State the blood parasite species.
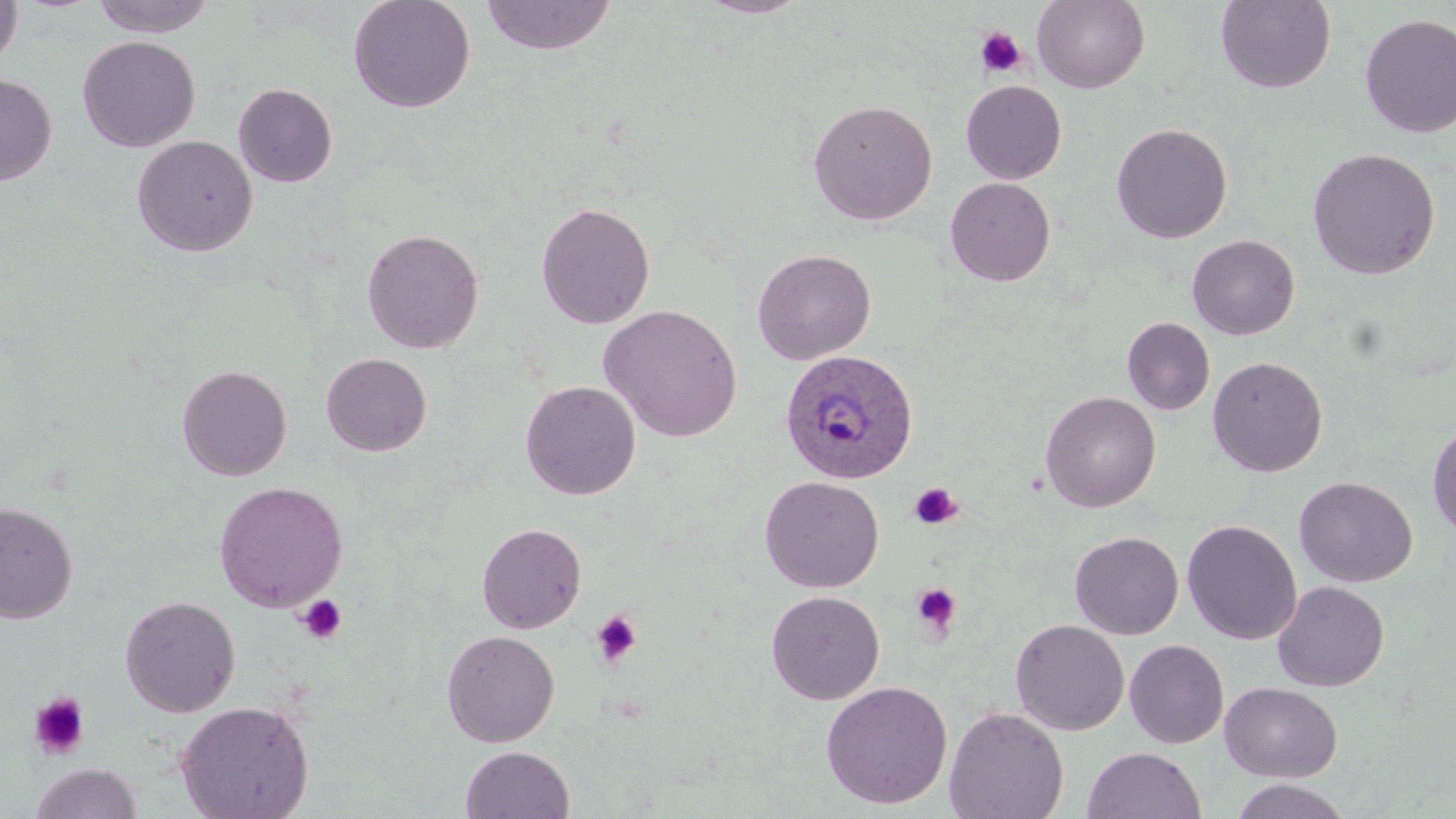
Plasmodium ovale.

Summary:
  - Coordinate format: approximate bounding boxes as [x1, y1, x2, y2] in pixels
  - Uninfected red blood cell locations: [0, 0, 23, 72], [90, 0, 218, 38], [348, 0, 476, 113], [481, 0, 617, 57], [694, 0, 813, 19], [1032, 0, 1150, 93], [1215, 1, 1336, 93], [1359, 13, 1456, 138], [77, 36, 201, 152], [0, 73, 57, 185], [961, 81, 1066, 184], [233, 83, 338, 187], [807, 98, 938, 226], [1111, 122, 1233, 244], [131, 135, 258, 256], [1306, 147, 1441, 280], [944, 177, 1055, 286], [535, 201, 656, 329], [361, 228, 485, 355], [1187, 234, 1300, 340], [752, 248, 877, 364], [599, 304, 742, 443], [1122, 317, 1215, 416], [320, 353, 432, 456], [1207, 355, 1328, 477], [176, 364, 293, 481], [520, 380, 641, 500], [1041, 390, 1161, 512], [1427, 419, 1456, 540], [759, 476, 884, 593], [1294, 476, 1418, 588], [213, 480, 349, 612], [0, 500, 78, 623], [1182, 519, 1302, 645], [476, 522, 587, 634], [1070, 531, 1184, 639], [1272, 581, 1389, 692], [766, 590, 886, 705], [119, 594, 241, 717], [1010, 618, 1130, 735], [441, 629, 560, 747], [1124, 639, 1229, 748], [820, 680, 953, 809], [1219, 681, 1343, 782], [175, 700, 315, 819], [944, 706, 1069, 819], [460, 746, 575, 819], [1082, 747, 1207, 819], [30, 763, 143, 819], [1228, 778, 1354, 819]
  - Platelet locations: [975, 27, 1027, 78], [909, 482, 962, 530], [910, 582, 963, 637], [294, 594, 348, 645], [590, 610, 643, 668], [28, 692, 91, 761]
  - Plasmodium ovale-infected red blood cell locations: [780, 348, 920, 485]
  - Field of view: one of a larger specimen
  - Image size: 1456×819 pixels
  - Preparation: thin blood film
  - Magnification: 1000x
  - Stain: May-Grünwald-Giemsa
  - Modality: light microscopy